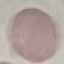

result = no malaria parasites detected
image type = cell patch, automatically extracted from a larger field of view and resized to 64 × 64 pixels
stain = Giemsa
capture = smartphone camera at the microscope eyepiece
preparation = thin smear